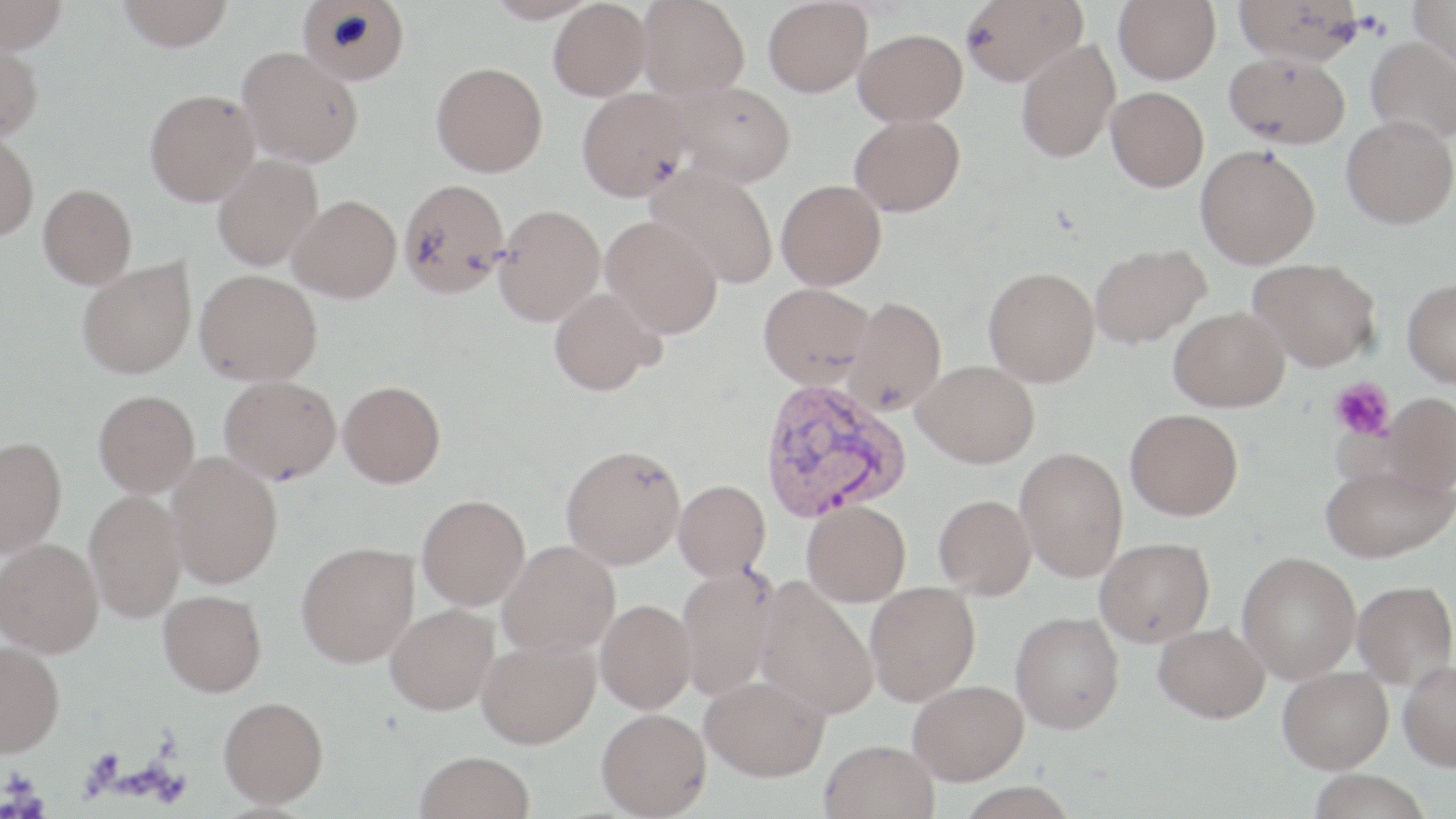
Summary:
  - Coordinate format: approximate bounding boxes as (x1,y1)-(x2,y2) corner pairs in pixels
  - Platelet locations: (1329,378)-(1395,441)
  - Plasmodium vivax-infected red blood cell locations: (759,379)-(911,522)
  - Uninfected red blood cell locations: (0,0)-(67,54), (117,0)-(234,51), (484,0)-(599,24), (637,0)-(750,100), (763,0)-(872,97), (960,0)-(1087,87), (1114,0)-(1221,85), (1233,0)-(1363,65), (1409,0)-(1456,72), (296,1)-(409,85), (548,1)-(651,101), (854,28)-(967,126), (1366,36)-(1456,144), (0,39)-(44,141), (1016,39)-(1120,163), (237,46)-(362,167), (1224,52)-(1350,148), (432,62)-(548,176), (672,81)-(796,187), (1106,86)-(1209,191), (577,87)-(693,202), (145,89)-(260,205), (849,114)-(965,217), (1341,115)-(1456,229), (0,130)-(39,241), (1196,145)-(1320,268), (212,154)-(323,271), (647,166)-(778,289), (398,178)-(509,299), (776,179)-(886,289), (38,184)-(137,288), (288,194)-(401,302), (495,204)-(605,325), (601,215)-(723,339), (1090,244)-(1210,349), (1248,258)-(1381,372), (77,259)-(196,378), (983,268)-(1099,387), (195,269)-(322,385), (1403,278)-(1456,387), (759,282)-(874,389), (549,287)-(663,396), (845,295)-(946,415), (1168,307)-(1289,412), (913,360)-(1040,468), (219,375)-(341,483), (338,380)-(445,487), (94,389)-(200,497), (1381,392)-(1456,495), (1125,408)-(1243,520), (0,436)-(67,557), (560,444)-(686,569), (1015,447)-(1128,581), (166,452)-(283,589), (1320,464)-(1453,563), (673,479)-(771,580), (84,489)-(187,623), (417,494)-(530,610), (934,494)-(1036,599), (802,499)-(911,606), (1095,537)-(1214,647), (0,538)-(103,657), (498,540)-(620,657), (296,542)-(419,667), (1237,551)-(1361,683), (676,564)-(781,701), (754,577)-(878,719), (1352,580)-(1455,688), (865,581)-(980,706), (158,590)-(267,696), (596,600)-(696,713), (385,603)-(499,715), (1010,611)-(1125,734), (1154,622)-(1270,723), (476,639)-(600,749), (0,641)-(64,756), (1398,660)-(1456,770), (1278,666)-(1393,773), (700,675)-(830,781), (908,679)-(1028,785), (219,696)-(328,807), (596,708)-(712,818), (820,739)-(940,819), (416,750)-(535,819), (1307,769)-(1433,819), (955,781)-(1078,819)
  - Slide-level diagnosis: Plasmodium vivax
  - Modality: optical microscopy
  - Image size: 1456×819 pixels
  - Field of view: one of a larger specimen
  - Magnification: 1000x
  - Preparation: thin blood smear
  - Stain: May-Grünwald-Giemsa